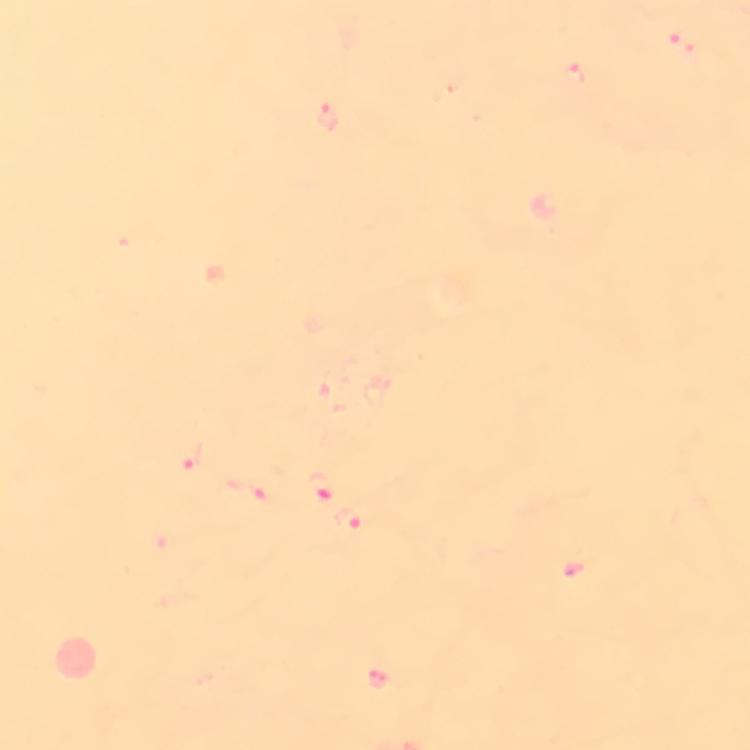

Approximate centers as [x, y] in pixels.
Summary:
  - Malaria parasite locations: [684, 47], [576, 77], [329, 117], [193, 456], [322, 488], [250, 490], [353, 519]
  - Image size: 750×750 pixels
  - Cropped from: a single field of view
  - Capture: smartphone mounted on the microscope
  - Stain: Giemsa
  - Preparation: thick blood film
  - Context: from a diagnostic examination for malaria
  - Magnification: 100x
  - Immersion oil: applied